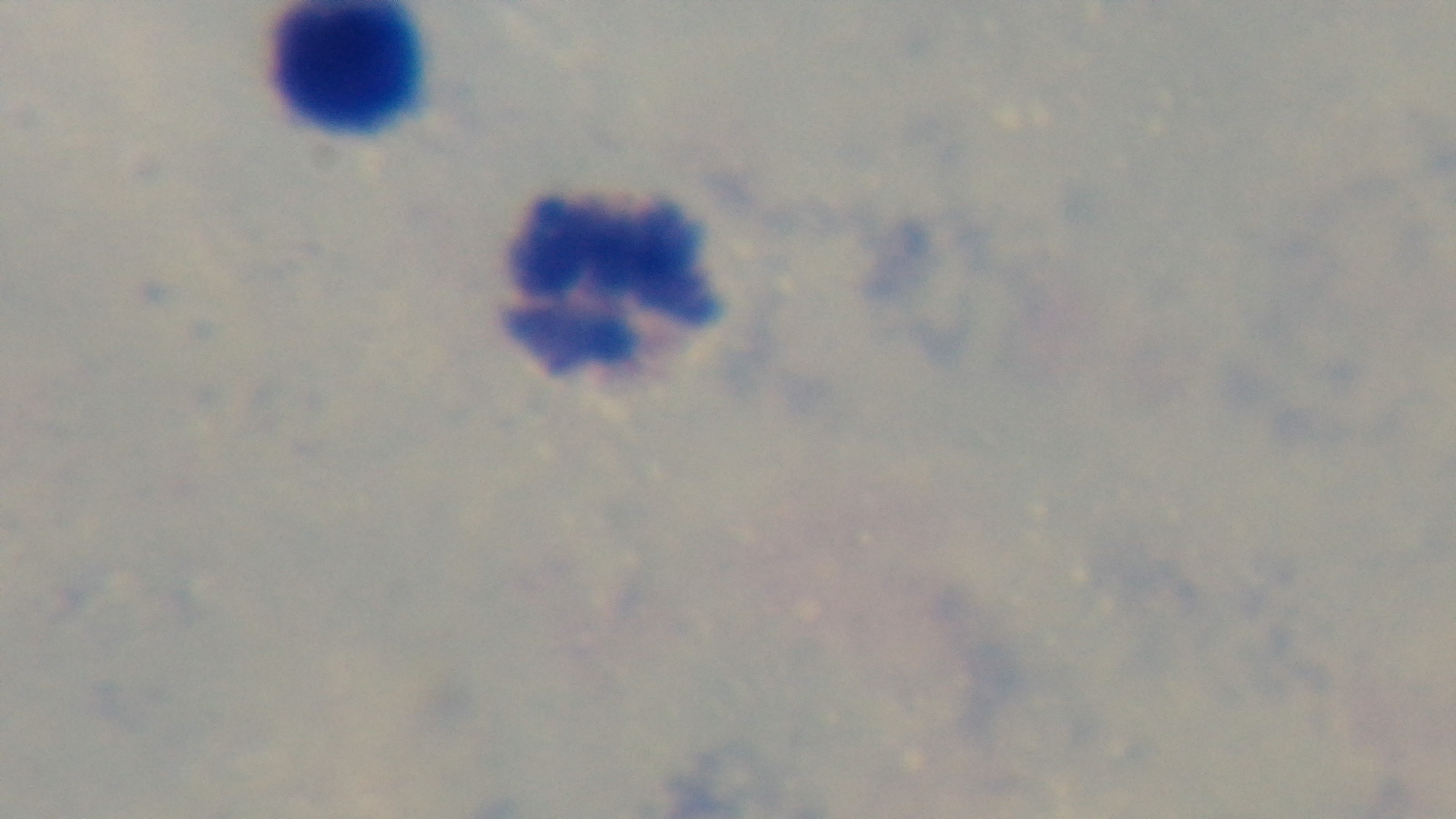
malaria status = uninfected
capture = mounted 4K digital camera
field of view = one from the slide
objective = 100x oil immersion
modality = light microscopy
stain = Giemsa
preparation = thick